Classify this cell by malaria status.
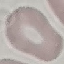

It is uninfected.

Thin smear of blood. Photographed with a smartphone camera at the microscope eyepiece. Automatically extracted cell patch, resized to 64 × 64 pixels. Giemsa stain.